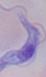

modality = micrograph
identification = trypanosome
magnification = 1000x